Name the parasite shown.
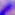
This is Toxoplasma gondii.

magnification = 400x
modality = micrograph